Report the malaria status of this cell.
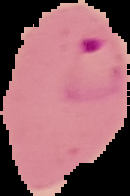
It is parasitized.

The area outside the segmented cell region is set to black. From a thin blood film. Image is 130×196 pixels.